Outline each blood parasite and name the species.
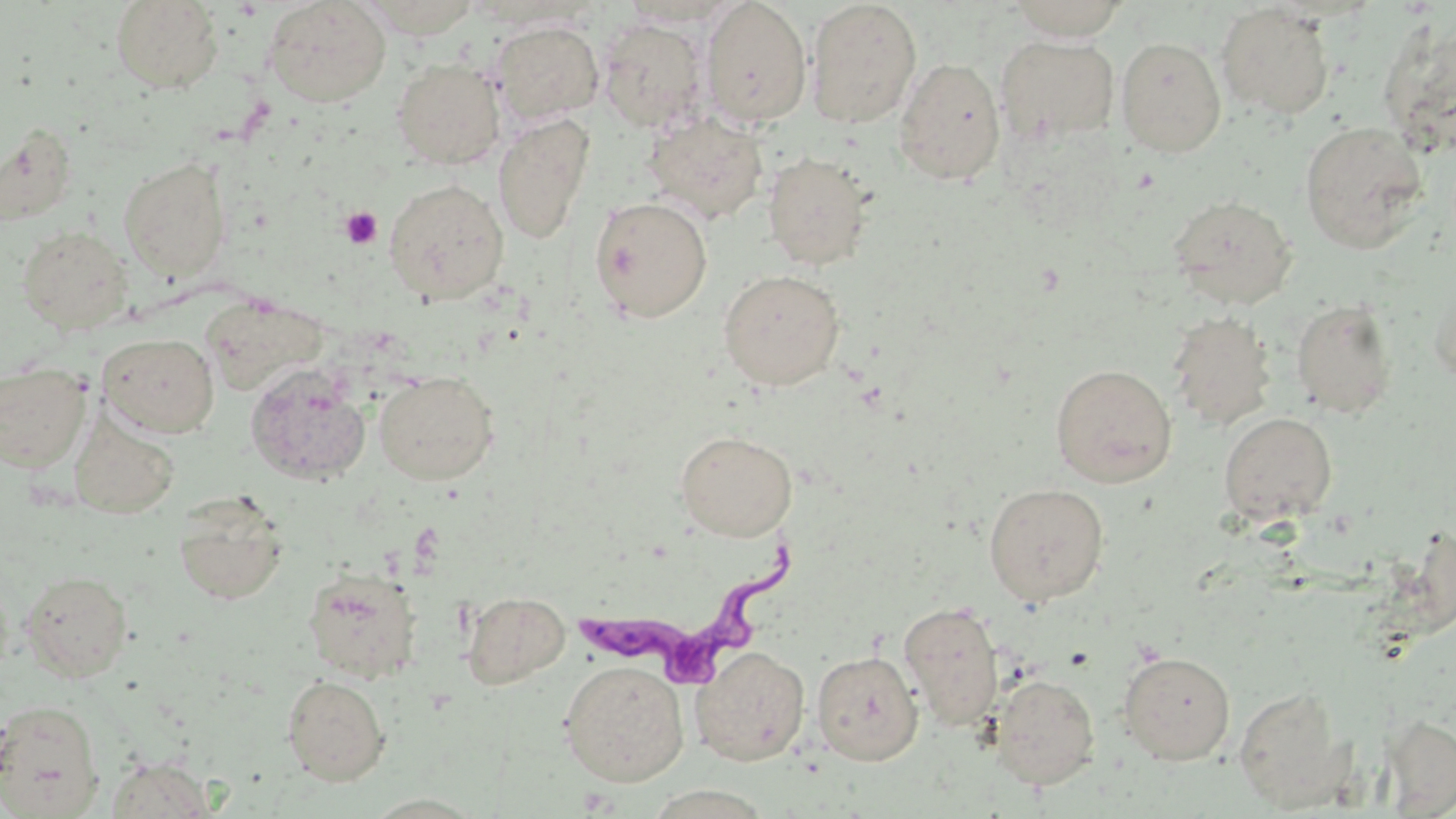

Approximate bounding boxes as (x1,y1)-(x2,y2) corner pairs in pixels.
Trypanosoma brucei: (575,546)-(798,694).
No Plasmodium falciparum, Plasmodium ovale, Plasmodium malariae, Plasmodium vivax, or Babesia divergens observed.

{
  "slide_level_diagnosis": "Trypanosoma brucei",
  "preparation": "thin blood film",
  "stain": "May-Grünwald-Giemsa",
  "image_size": "1456×819 pixels",
  "field_of_view": "one of a larger specimen",
  "platelet_locations": "approximate bounding boxes as (x1,y1)-(x2,y2) corner pairs in pixels: (340,206)-(383,249)",
  "magnification": "1000x",
  "uninfected_red_blood_cell_locations": "approximate bounding boxes as (x1,y1)-(x2,y2) corner pairs in pixels: (263,0)-(392,108), (358,0)-(482,38), (700,0)-(812,127), (805,0)-(922,128), (1007,0)-(1130,40), (111,1)-(223,93), (620,1)-(749,29), (1216,4)-(1335,119), (1377,17)-(1456,157), (597,18)-(710,133), (489,20)-(604,125), (996,34)-(1120,145), (1115,36)-(1227,157), (894,57)-(1006,185), (391,58)-(505,169), (643,111)-(768,223), (493,113)-(595,245), (1299,122)-(1428,252), (1,124)-(79,225), (763,151)-(874,270), (118,157)-(231,282), (383,177)-(509,304), (1168,195)-(1298,308), (589,196)-(713,322), (17,224)-(134,333), (718,269)-(846,390), (1428,275)-(1456,386), (200,297)-(328,397), (1290,298)-(1399,419), (1167,310)-(1277,431), (97,333)-(219,437), (0,363)-(91,473), (245,363)-(372,486), (1050,364)-(1177,487), (374,371)-(500,485), (1219,412)-(1338,525), (68,413)-(181,520), (675,430)-(798,541), (983,482)-(1110,606), (173,492)-(288,605), (302,565)-(422,683), (20,569)-(133,682), (462,592)-(569,688), (898,601)-(1005,730), (690,645)-(811,765), (811,649)-(924,765), (1118,650)-(1236,763), (559,660)-(689,787), (991,673)-(1100,790), (282,674)-(391,785), (1233,684)-(1353,811), (0,699)-(104,817), (1380,715)-(1455,813), (104,757)-(217,818), (361,794)-(490,817)",
  "modality": "optical microscopy"
}